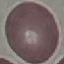

Summary:
  - Malaria status: uninfected
  - Capture: smartphone through the microscope eyepiece
  - Stain: Giemsa
  - Image type: cell patch, automatically extracted from a larger field of view and resized to 64 × 64 pixels
  - Preparation: thin blood smear